Classify this cell by malaria status.
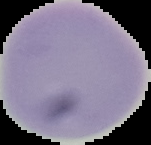

It is uninfected.

Cell region segmented out of the field of view; the surrounding area is masked to black. Image is 151×145 pixels. From a thin blood film.